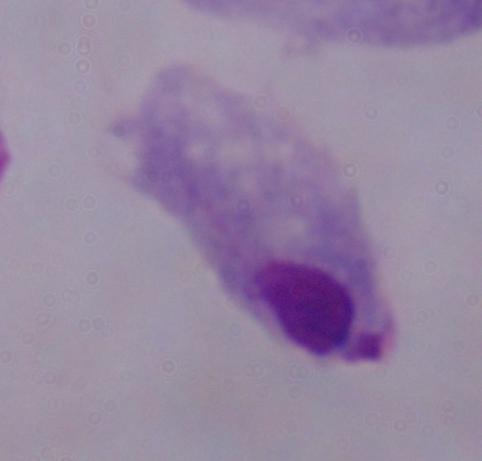 A trichomonad is shown. Captured at 1000x magnification. Photomicrograph.